Assess this cell for malaria.
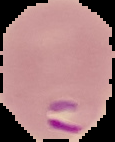

Parasitized.

Cell region segmented out of the field of view; the surrounding area is masked to black. Image is 115×142 pixels. From a thin blood film.